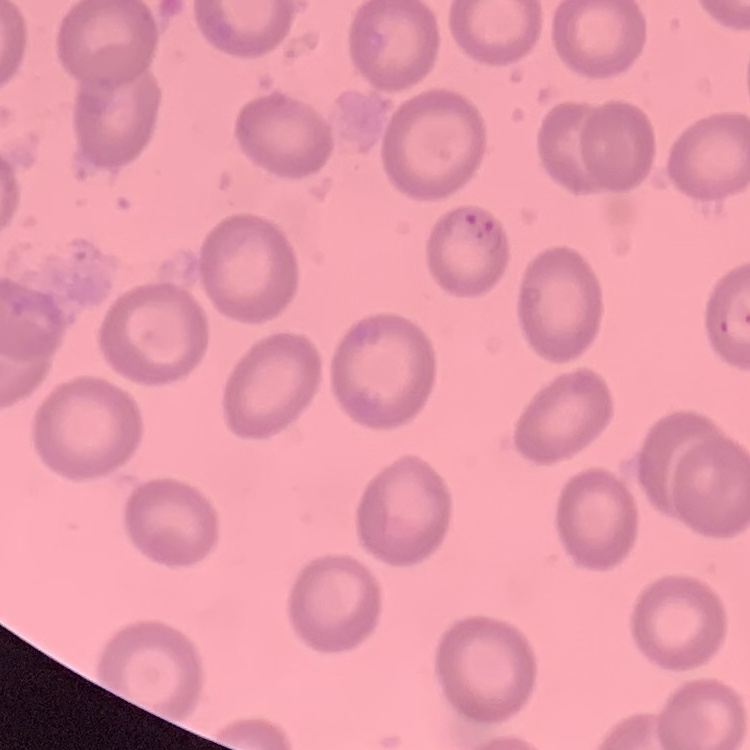
Summary:
  - Red blood cell morphology: no rouleaux formation
  - Stain: Field's or Giemsa
  - Image type: one tile cut from a larger photomicrograph
  - Preparation: thin blood film